Identify the preparation type.
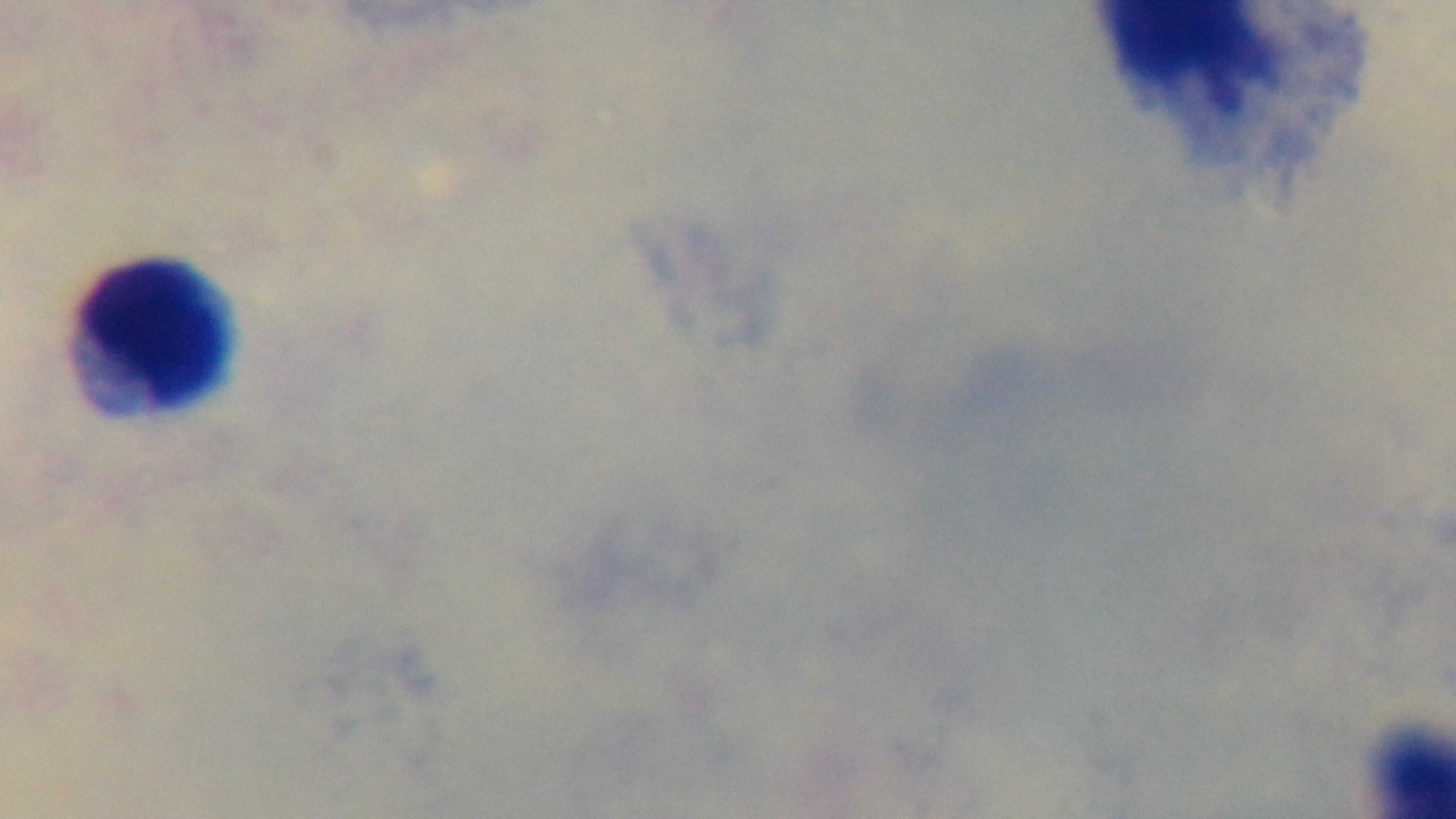

Thick.

100x oil-immersion objective. Single field of view. Giemsa stain. Malaria status: uninfected. Photomicrograph. Mounted 4K digital camera.